Assess this cell for malaria.
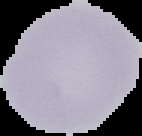
Uninfected.

Cell region segmented out of the field of view; the surrounding area is masked to black. From a thin blood film. Image is 142×136 pixels.